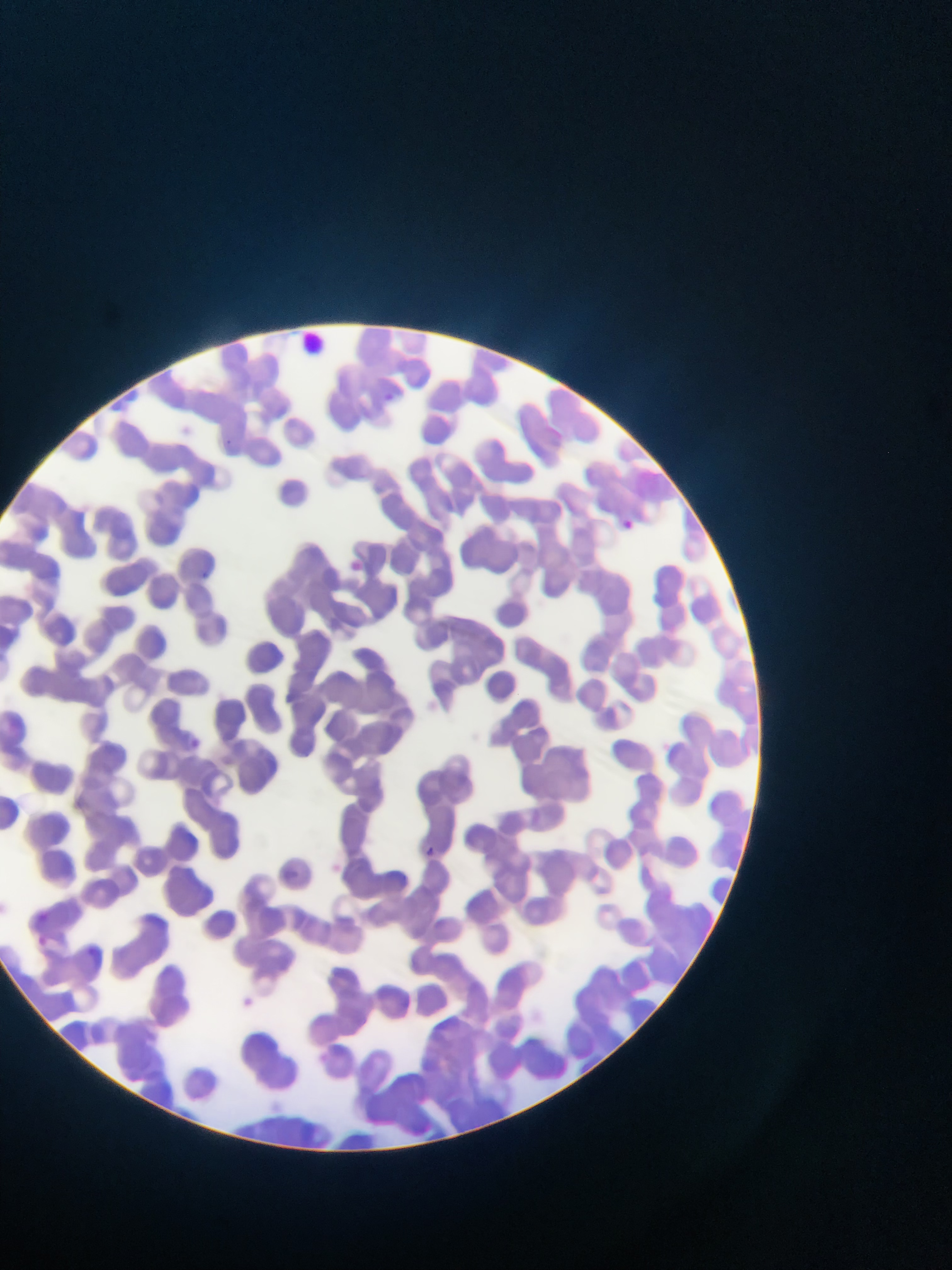
Approximate bounding boxes as left top right bottom in pixels. Malaria parasite locations: 618 515 635 538; 421 844 444 857. Image is 952×1270 pixels. Photographed through a microscope with a mobile-phone camera. One field of view. Thin blood smear. Sample from Ghana.